Outline each blood parasite and name the species.
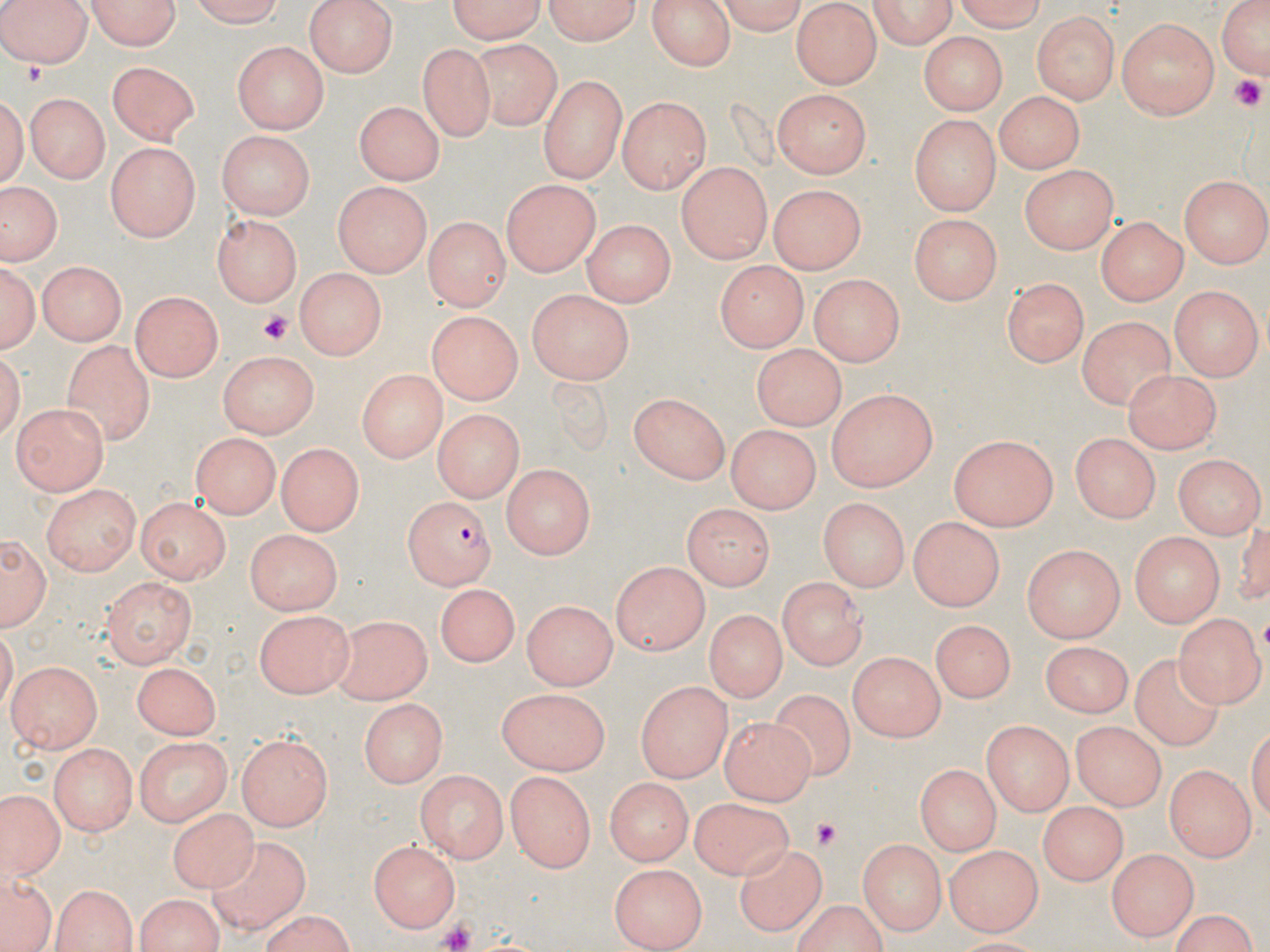

Approximate bounding boxes as [x1, y1, x2, y2] in pixels.
Plasmodium falciparum-infected red blood cells: [401, 495, 496, 587].
No Plasmodium ovale, Plasmodium malariae, Plasmodium vivax, Babesia divergens, or Trypanosoma brucei observed.

slide-level diagnosis = Plasmodium falciparum
preparation = thin blood film
uninfected red blood cell locations = approximate bounding boxes as [x1, y1, x2, y2] in pixels: [3, 0, 92, 68], [81, 0, 183, 50], [189, 0, 293, 27], [303, 0, 400, 76], [442, 0, 549, 40], [540, 0, 643, 45], [644, 0, 737, 71], [867, 0, 959, 48], [952, 0, 1052, 30], [1214, 0, 1270, 80], [719, 1, 808, 34], [794, 1, 878, 88], [1032, 11, 1117, 104], [1117, 17, 1220, 120], [920, 33, 1003, 112], [232, 39, 327, 132], [470, 39, 559, 128], [418, 43, 495, 142], [107, 61, 198, 145], [539, 76, 626, 181], [0, 82, 27, 192], [772, 89, 868, 177], [992, 90, 1082, 172], [24, 93, 111, 182], [616, 96, 711, 191], [356, 101, 445, 186], [908, 113, 1001, 214], [216, 131, 316, 221], [104, 141, 198, 244], [675, 161, 772, 261], [1018, 164, 1119, 250], [1182, 176, 1269, 268], [503, 179, 601, 279], [332, 181, 430, 277], [767, 184, 864, 271], [2, 187, 58, 263], [909, 214, 1002, 302], [212, 215, 301, 305], [1097, 216, 1187, 303], [424, 218, 508, 313], [583, 219, 672, 308], [0, 260, 41, 358], [39, 260, 128, 346], [715, 261, 810, 348], [296, 267, 388, 357], [811, 274, 904, 365], [998, 280, 1088, 365], [1168, 286, 1259, 380], [524, 290, 632, 385], [133, 291, 223, 379], [426, 310, 520, 404], [1081, 317, 1174, 410], [62, 341, 155, 447], [750, 344, 844, 428], [218, 352, 319, 437], [358, 367, 447, 461], [1126, 368, 1226, 453], [826, 387, 937, 492], [627, 392, 732, 483], [11, 403, 107, 494], [435, 411, 520, 502], [726, 425, 818, 515], [193, 431, 280, 517], [1070, 432, 1161, 521], [950, 434, 1061, 531], [276, 443, 365, 534], [1172, 454, 1264, 540], [503, 465, 594, 559], [40, 484, 142, 576], [134, 496, 232, 580], [820, 498, 909, 592], [681, 500, 772, 589], [907, 516, 1006, 612], [247, 529, 343, 614], [2, 530, 49, 633], [1125, 531, 1224, 628], [1022, 542, 1125, 641], [609, 561, 707, 654], [777, 574, 868, 668], [101, 576, 197, 663], [437, 582, 522, 665], [523, 600, 616, 688], [255, 609, 355, 697], [1175, 611, 1264, 707], [704, 612, 784, 705], [331, 613, 431, 704], [937, 616, 1014, 699], [1042, 641, 1130, 717], [847, 651, 943, 740], [1129, 655, 1221, 751], [7, 661, 102, 753], [134, 661, 221, 739], [637, 679, 734, 780], [495, 689, 611, 774], [769, 693, 857, 781], [356, 699, 448, 787], [721, 718, 815, 802], [983, 721, 1074, 818], [1071, 722, 1162, 809], [131, 734, 234, 821], [236, 735, 334, 832], [50, 743, 140, 835], [913, 765, 1002, 853], [1165, 766, 1253, 860], [417, 770, 507, 862], [505, 770, 593, 873], [606, 778, 690, 863], [4, 793, 58, 880], [692, 797, 792, 877], [169, 800, 256, 894], [1037, 802, 1129, 883], [205, 834, 310, 933], [858, 838, 945, 934], [369, 839, 463, 934], [944, 844, 1040, 934], [738, 847, 827, 933], [1108, 848, 1196, 942], [606, 862, 709, 946], [1, 870, 55, 952], [49, 884, 140, 952], [133, 892, 226, 951], [791, 901, 890, 952], [1166, 909, 1261, 951], [258, 913, 357, 951]
image size = 1270×952 pixels
field of view = one of a larger specimen
magnification = 1000x
stain = May-Grünwald-Giemsa
platelet locations = approximate bounding boxes as [x1, y1, x2, y2] in pixels: [1227, 74, 1268, 110], [259, 308, 295, 342], [807, 818, 843, 850], [434, 918, 479, 952]
modality = optical microscopy